Assess this cell for malaria.
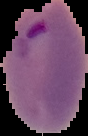

Parasitized.

The area outside the segmented cell region is set to black. Image is 88×136 pixels. From a thin blood smear.